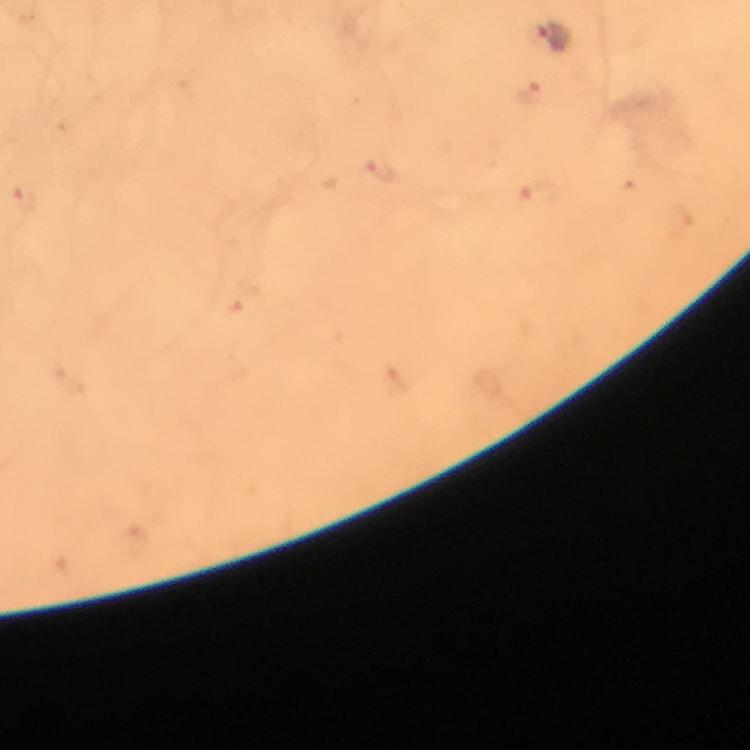

Approximate object centers, in pixels from the top-left corner. Malaria parasite locations: (x=554, y=36), (x=535, y=92), (x=380, y=171), (x=540, y=195), (x=26, y=198), (x=243, y=301). Smartphone photograph taken through a microscope. Thick blood smear. Immersion oil applied. From a malaria diagnostic workup. Giemsa-stained preparation. Image is 750×750 pixels. At 100x magnification. Cropped region of a single field of view.